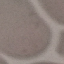

{
  "malaria_status": "uninfected",
  "capture": "smartphone camera at the microscope eyepiece",
  "stain": "Giemsa",
  "preparation": "thin blood smear",
  "image_type": "cell patch, automatically extracted from a larger field of view and resized to 64 × 64 pixels"
}